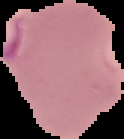

Summary:
  - Image type: segmented cell region with the area outside set to black
  - Malaria status: parasitized
  - Preparation: thin blood smear
  - Image size: 124×139 pixels